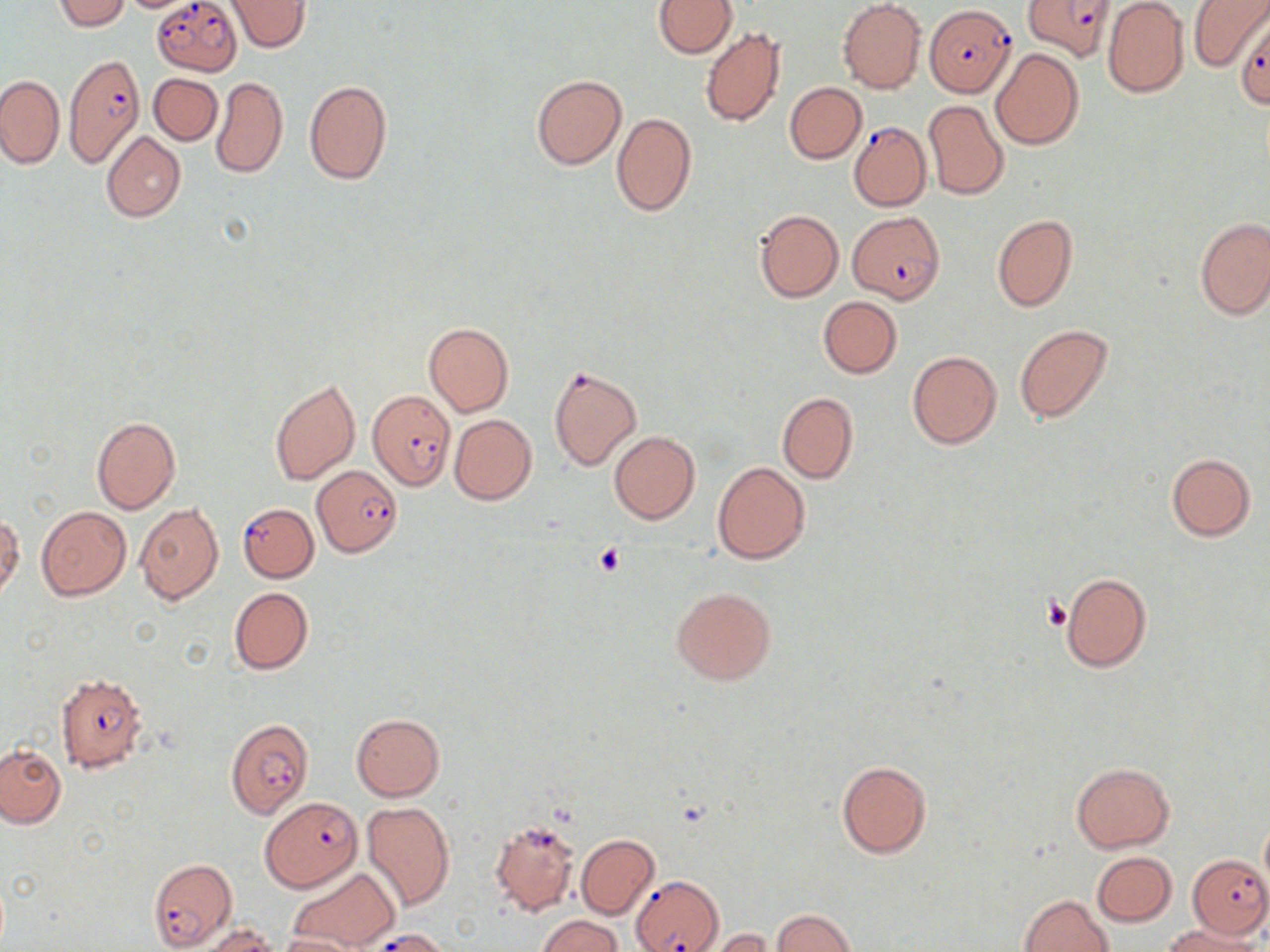

{
  "slide_level_diagnosis": "Plasmodium falciparum",
  "image_size": "1270×952 pixels",
  "stain": "May-Grünwald-Giemsa",
  "preparation": "thin blood film",
  "field_of_view": "one of a larger specimen",
  "modality": "light microscopy",
  "uninfected_red_blood_cell_locations": "approximate bounding boxes as [x1, y1, x2, y2] in pixels: [53, 0, 132, 32], [227, 0, 312, 53], [653, 0, 735, 58], [837, 0, 927, 93], [1187, 0, 1268, 71], [1102, 2, 1190, 98], [700, 27, 786, 127], [991, 48, 1084, 152], [149, 72, 222, 144], [0, 75, 64, 168], [531, 75, 625, 169], [211, 76, 288, 179], [303, 79, 392, 185], [784, 82, 866, 164], [923, 99, 1008, 200], [612, 113, 697, 216], [101, 131, 186, 222], [755, 210, 843, 302], [992, 213, 1078, 313], [1194, 217, 1270, 320], [819, 297, 902, 377], [423, 322, 514, 417], [1014, 324, 1115, 425], [908, 351, 1002, 450], [270, 378, 360, 485], [776, 392, 859, 484], [90, 415, 181, 514], [449, 415, 537, 504], [609, 431, 700, 525], [1166, 453, 1256, 541], [713, 462, 810, 564], [134, 503, 223, 604], [36, 506, 132, 600], [1, 513, 23, 601], [1060, 572, 1153, 673], [672, 586, 776, 686], [229, 587, 313, 675], [350, 713, 446, 801], [0, 743, 68, 828], [836, 759, 932, 859], [1070, 762, 1175, 852], [362, 801, 456, 912], [1259, 816, 1270, 898], [576, 833, 659, 920], [1091, 851, 1177, 927], [287, 866, 399, 950], [1020, 894, 1114, 952], [771, 908, 859, 950], [537, 915, 622, 952], [1163, 923, 1264, 952], [193, 924, 277, 952], [705, 929, 775, 952], [277, 933, 367, 952]",
  "magnification": "1000x",
  "platelet_locations": "approximate bounding boxes as [x1, y1, x2, y2] in pixels: [594, 544, 627, 575], [1045, 596, 1074, 632]",
  "plasmodium_falciparum_infected_red_blood_cell_locations": "approximate bounding boxes as [x1, y1, x2, y2] in pixels: [1022, 0, 1113, 62], [152, 2, 242, 74], [927, 4, 1015, 95], [1234, 15, 1270, 110], [63, 53, 143, 171], [848, 120, 932, 212], [847, 213, 945, 305], [547, 365, 642, 470], [366, 387, 456, 489], [313, 466, 402, 557], [237, 502, 319, 582], [56, 673, 147, 773], [224, 717, 314, 820], [261, 797, 362, 892], [496, 821, 575, 918], [1187, 854, 1270, 938], [147, 859, 237, 949], [630, 874, 724, 952]"
}